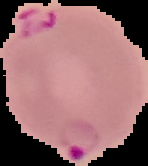 From a thin blood smear. Image is 148×166 pixels. Malaria status: parasitized. The area outside the segmented cell region is set to black.